Name the cell type shown.
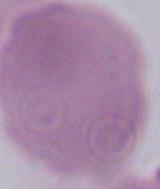
This is an erythrocyte.

Photomicrograph. 1000x magnification.